State the preparation type.
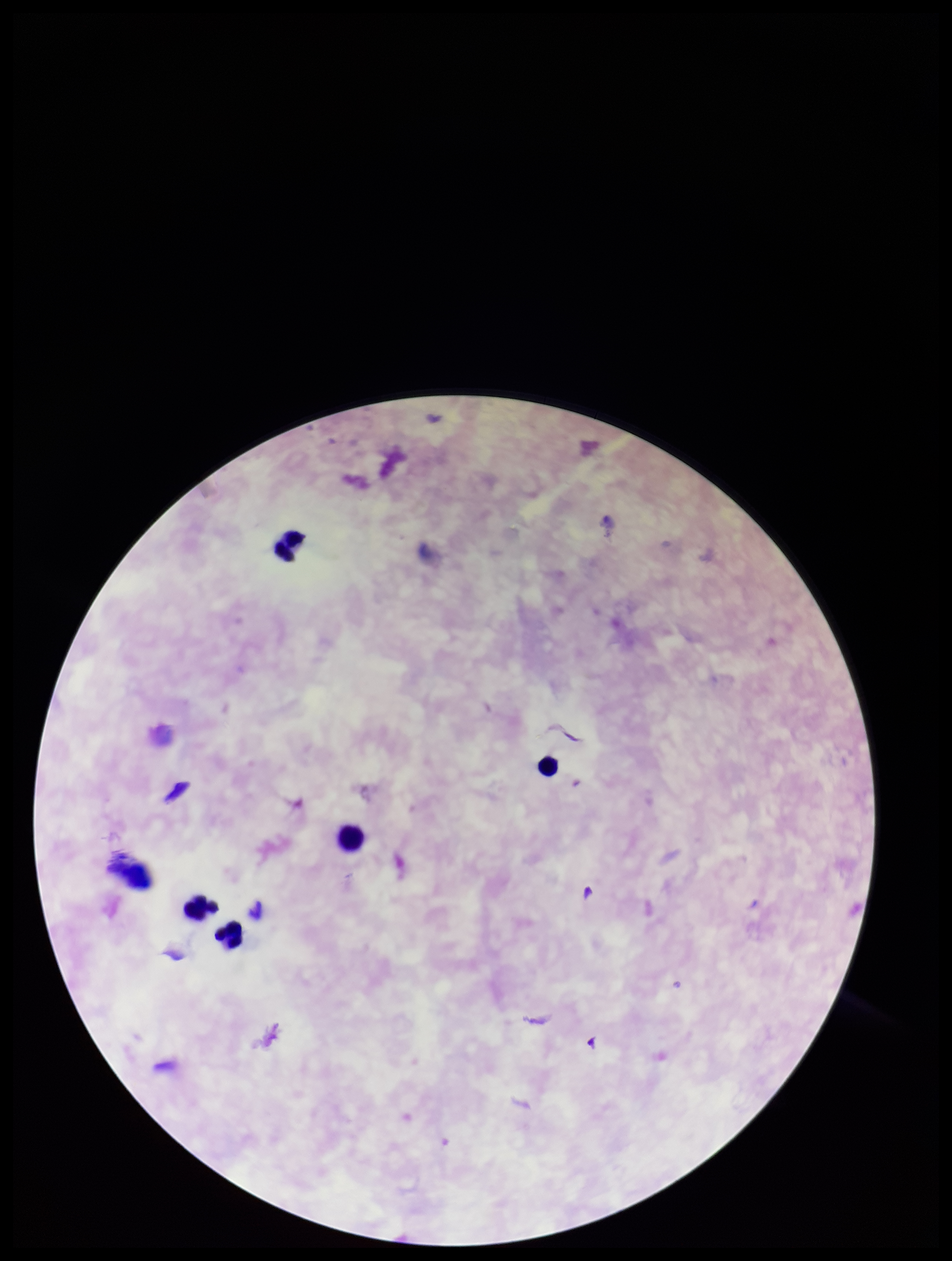
It is a thick blood smear.

Parasite count: 0. Image is 952×1261 pixels. Patient malaria status: negative. Plasmodium parasites: none identified. Giemsa stain. One field from this slide. Smartphone photograph taken through the eyepiece of a microscope. Leukocyte count: 5.